Locate every Plasmodium parasite.
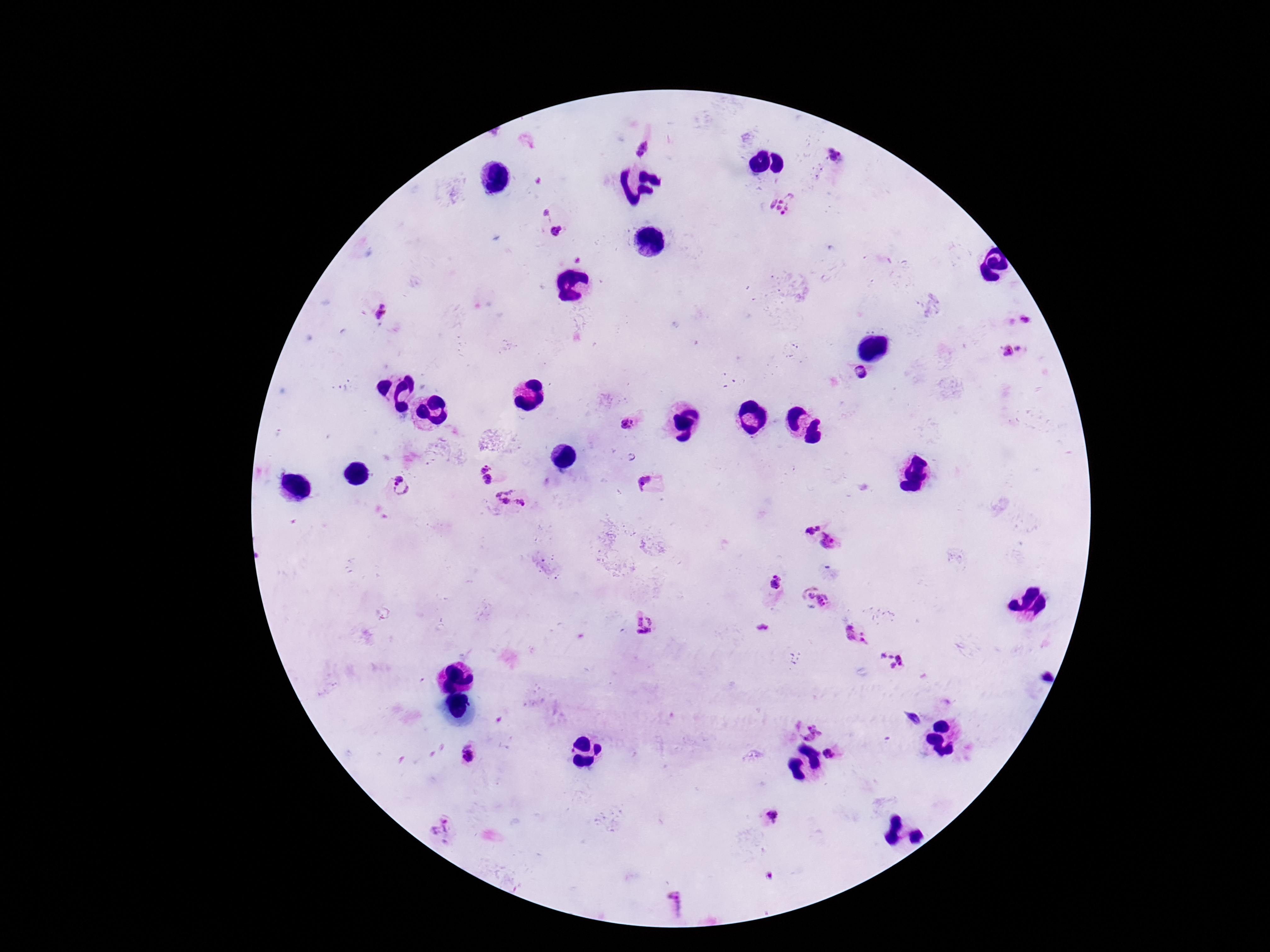
Approximate object centers, in pixels from the top-left corner.
Plasmodium parasites: (x=642, y=148), (x=833, y=156), (x=784, y=204), (x=547, y=213), (x=555, y=231), (x=380, y=312), (x=1027, y=319), (x=1019, y=349), (x=1008, y=351), (x=862, y=372), (x=628, y=423), (x=484, y=468), (x=399, y=477), (x=487, y=480), (x=648, y=484), (x=400, y=490), (x=511, y=499), (x=808, y=524), (x=832, y=542), (x=777, y=581), (x=811, y=596), (x=823, y=599), (x=645, y=624), (x=856, y=635), (x=890, y=659), (x=913, y=719), (x=808, y=731), (x=467, y=754), (x=826, y=755), (x=770, y=817), (x=441, y=831), (x=677, y=904).

magnification = 100x
field of view = single
preparation = thick peripheral-blood smear
image size = 1270×952 pixels
stain = Giemsa
capture = smartphone camera through the microscope eyepiece
patient malaria status = infected